Assess this cell for malaria.
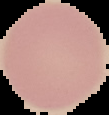
It is uninfected.

Summary:
  - Preparation: thin blood film
  - Image type: segmented cell region with the area outside set to black
  - Image size: 109×115 pixels